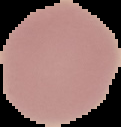
preparation = thin blood film
result = negative for malaria parasites
image size = 121×127 pixels
image type = segmented cell region with the area outside set to black